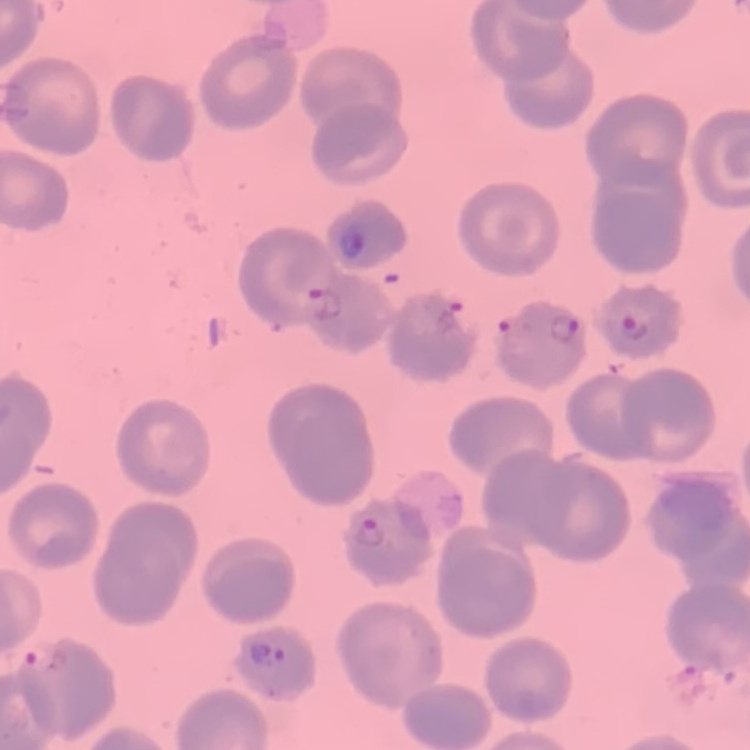

red blood cell morphology = no rouleaux formation
image type = square crop of a larger photomicrograph
stain = Field's or Giemsa
preparation = thin blood film